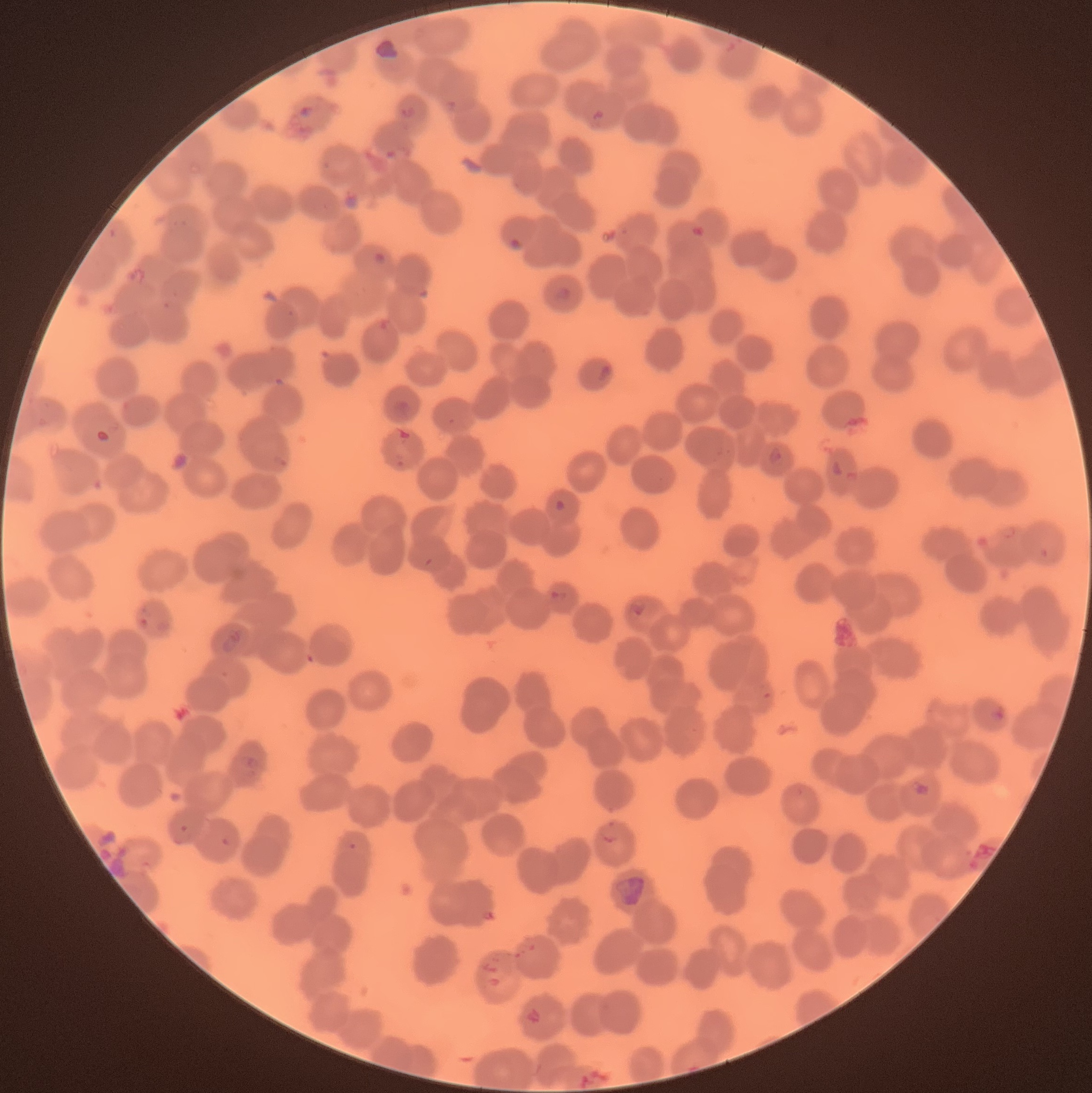
coordinate format = approximate bounding boxes as (x1,y1)-(x2,y2) corner pairs in pixels
Plasmodium parasite locations = (297,104)-(313,118), (401,105)-(417,121), (590,107)-(607,124), (507,235)-(527,254), (125,266)-(147,286), (554,287)-(573,300), (598,361)-(612,382), (766,446)-(783,463), (830,458)-(845,478), (551,496)-(568,514), (549,589)-(568,604), (628,601)-(647,619), (220,630)-(245,652), (989,705)-(1007,723), (241,754)-(263,773), (912,781)-(932,797), (178,824)-(190,835), (218,837)-(232,848), (347,842)-(359,852), (475,906)-(496,923)
image size = 1092×1093 pixels
modality = optical microscopy
red blood cell morphology = rouleaux formation
preparation = thin blood film